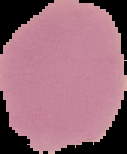

image size = 127×154 pixels
image type = cell region segmented out of the field of view; surrounding area masked to black
preparation = thin blood smear
malaria status = uninfected